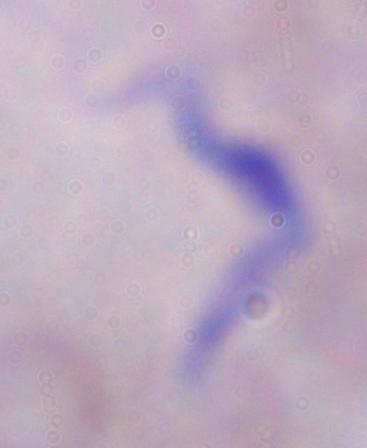
Summary:
  - Modality: micrograph
  - Identification: trypanosome
  - Magnification: 1000x